Classify this cell by malaria status.
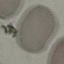

It is uninfected.

Thin smear of blood. Acquired by smartphone through the microscope eyepiece. Giemsa stain. Cell patch, automatically extracted from a larger field of view and resized to 64 × 64 pixels.